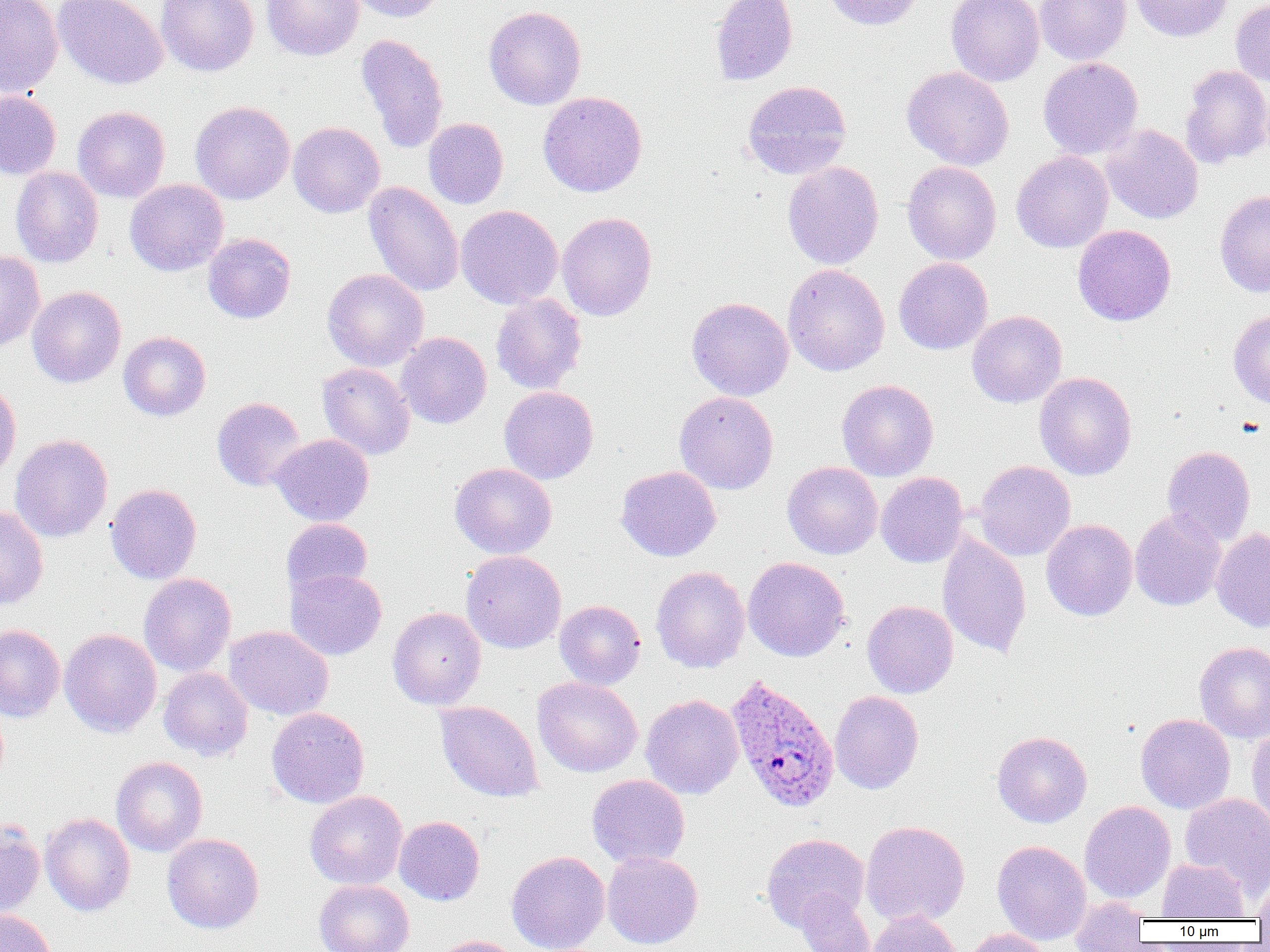 Approximate bounding boxes as named x1/y1/x2/y2 corners in pixels. Plasmodium ovale-infected red blood cell locations: (x1=725, y1=674, x2=840, y2=814). Uninfected red blood cell locations: (x1=0, y1=0, x2=63, y2=98), (x1=53, y1=0, x2=167, y2=90), (x1=157, y1=0, x2=260, y2=77), (x1=262, y1=0, x2=363, y2=61), (x1=346, y1=0, x2=448, y2=23), (x1=710, y1=0, x2=798, y2=86), (x1=824, y1=0, x2=925, y2=30), (x1=947, y1=0, x2=1045, y2=86), (x1=1035, y1=0, x2=1131, y2=65), (x1=1130, y1=0, x2=1233, y2=42), (x1=1231, y1=0, x2=1270, y2=87), (x1=484, y1=6, x2=586, y2=109), (x1=355, y1=33, x2=449, y2=154), (x1=1039, y1=57, x2=1143, y2=160), (x1=1180, y1=65, x2=1270, y2=168), (x1=901, y1=66, x2=1014, y2=171), (x1=742, y1=81, x2=852, y2=180), (x1=0, y1=90, x2=61, y2=180), (x1=537, y1=91, x2=648, y2=197), (x1=190, y1=100, x2=295, y2=204), (x1=73, y1=105, x2=170, y2=203), (x1=423, y1=118, x2=509, y2=209), (x1=288, y1=121, x2=385, y2=218), (x1=1101, y1=125, x2=1203, y2=224), (x1=1011, y1=150, x2=1113, y2=253), (x1=782, y1=161, x2=884, y2=270), (x1=902, y1=161, x2=1001, y2=265), (x1=10, y1=166, x2=104, y2=268), (x1=125, y1=178, x2=229, y2=276), (x1=364, y1=181, x2=464, y2=297), (x1=1215, y1=190, x2=1270, y2=297), (x1=455, y1=204, x2=563, y2=309), (x1=557, y1=211, x2=657, y2=321), (x1=1072, y1=224, x2=1176, y2=326), (x1=203, y1=233, x2=296, y2=324), (x1=0, y1=250, x2=45, y2=353), (x1=893, y1=257, x2=993, y2=355), (x1=782, y1=264, x2=890, y2=376), (x1=322, y1=268, x2=429, y2=371), (x1=27, y1=286, x2=126, y2=387), (x1=490, y1=293, x2=587, y2=395), (x1=686, y1=297, x2=794, y2=401), (x1=967, y1=310, x2=1067, y2=408), (x1=1228, y1=310, x2=1270, y2=408), (x1=119, y1=331, x2=211, y2=421), (x1=395, y1=332, x2=492, y2=428), (x1=317, y1=362, x2=415, y2=459), (x1=1035, y1=372, x2=1137, y2=481), (x1=836, y1=379, x2=939, y2=481), (x1=0, y1=380, x2=21, y2=486), (x1=499, y1=386, x2=598, y2=484), (x1=675, y1=392, x2=779, y2=494), (x1=212, y1=397, x2=306, y2=491), (x1=10, y1=433, x2=112, y2=542), (x1=270, y1=434, x2=374, y2=526), (x1=1162, y1=445, x2=1255, y2=545), (x1=974, y1=460, x2=1076, y2=561), (x1=782, y1=461, x2=882, y2=559), (x1=449, y1=463, x2=557, y2=559), (x1=616, y1=466, x2=722, y2=561), (x1=876, y1=472, x2=968, y2=568), (x1=106, y1=483, x2=202, y2=584), (x1=0, y1=505, x2=48, y2=609), (x1=1130, y1=509, x2=1226, y2=611), (x1=281, y1=518, x2=373, y2=599), (x1=1041, y1=519, x2=1138, y2=621), (x1=1211, y1=527, x2=1270, y2=632), (x1=937, y1=532, x2=1032, y2=659), (x1=461, y1=550, x2=566, y2=654), (x1=742, y1=557, x2=850, y2=662), (x1=651, y1=565, x2=750, y2=673), (x1=286, y1=569, x2=387, y2=660), (x1=139, y1=573, x2=236, y2=677), (x1=554, y1=600, x2=646, y2=689), (x1=862, y1=600, x2=959, y2=698), (x1=388, y1=606, x2=486, y2=710), (x1=0, y1=623, x2=65, y2=722), (x1=224, y1=626, x2=334, y2=721), (x1=59, y1=628, x2=162, y2=737), (x1=1194, y1=642, x2=1270, y2=743), (x1=158, y1=667, x2=253, y2=761), (x1=532, y1=676, x2=642, y2=777), (x1=829, y1=691, x2=924, y2=794), (x1=640, y1=694, x2=743, y2=799), (x1=435, y1=701, x2=543, y2=802), (x1=266, y1=707, x2=370, y2=808), (x1=1135, y1=713, x2=1235, y2=814), (x1=1247, y1=726, x2=1270, y2=833), (x1=992, y1=730, x2=1092, y2=827), (x1=111, y1=755, x2=208, y2=857), (x1=587, y1=774, x2=690, y2=868), (x1=305, y1=790, x2=407, y2=890), (x1=1180, y1=793, x2=1270, y2=894), (x1=1079, y1=800, x2=1176, y2=903), (x1=40, y1=813, x2=136, y2=916), (x1=394, y1=815, x2=484, y2=906), (x1=0, y1=819, x2=45, y2=919), (x1=860, y1=820, x2=970, y2=927), (x1=162, y1=833, x2=264, y2=934), (x1=761, y1=833, x2=869, y2=932), (x1=992, y1=840, x2=1091, y2=944), (x1=506, y1=850, x2=610, y2=952), (x1=602, y1=850, x2=703, y2=949), (x1=1158, y1=858, x2=1249, y2=921), (x1=1254, y1=869, x2=1270, y2=924), (x1=314, y1=879, x2=414, y2=952), (x1=795, y1=889, x2=878, y2=952), (x1=1068, y1=897, x2=1150, y2=951), (x1=0, y1=909, x2=57, y2=952), (x1=866, y1=910, x2=961, y2=952), (x1=962, y1=928, x2=1053, y2=952), (x1=431, y1=935, x2=523, y2=952). Slide-level diagnosis: Plasmodium ovale. Image is 1270×952 pixels. Captured at 1000x magnification. Thin blood film. Single field of view. Optical microscopy.